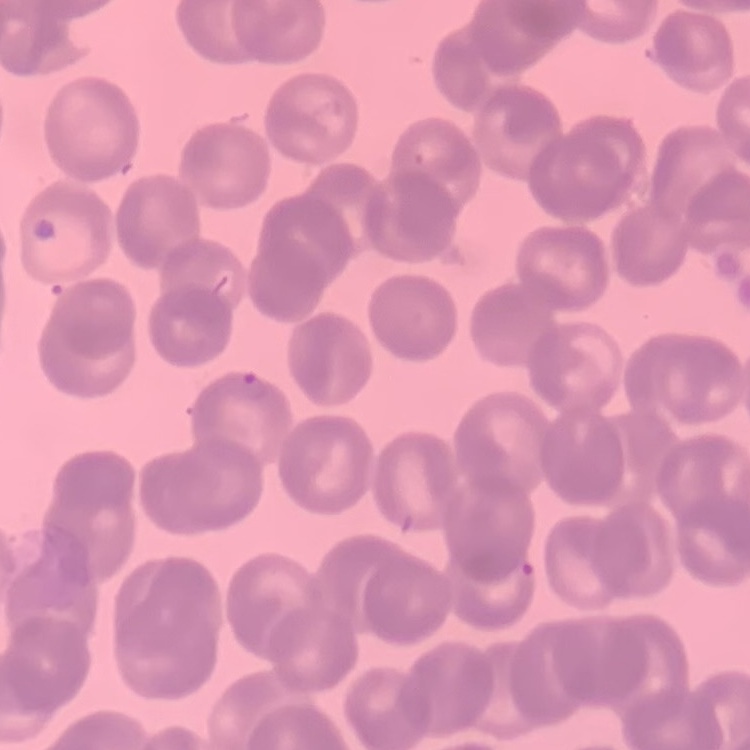
The red blood cells exhibit rouleaux formation. Field's or Giemsa stain. Thin blood film. One tile cut from a larger photomicrograph.